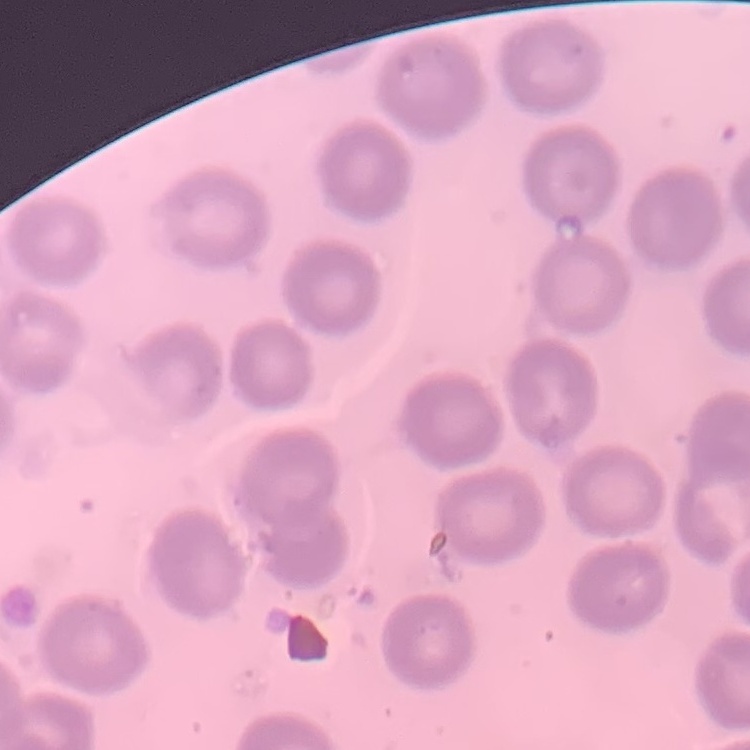

Summary:
  - Red blood cell morphology: no rouleaux formation
  - Stain: Field's or Giemsa
  - Image type: one tile cut from a larger photomicrograph
  - Preparation: thin peripheral smear